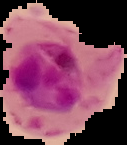
From a thin blood film. Result: malaria parasites detected. Cell region segmented out of the field of view; the surrounding area is masked to black. Image is 127×145 pixels.